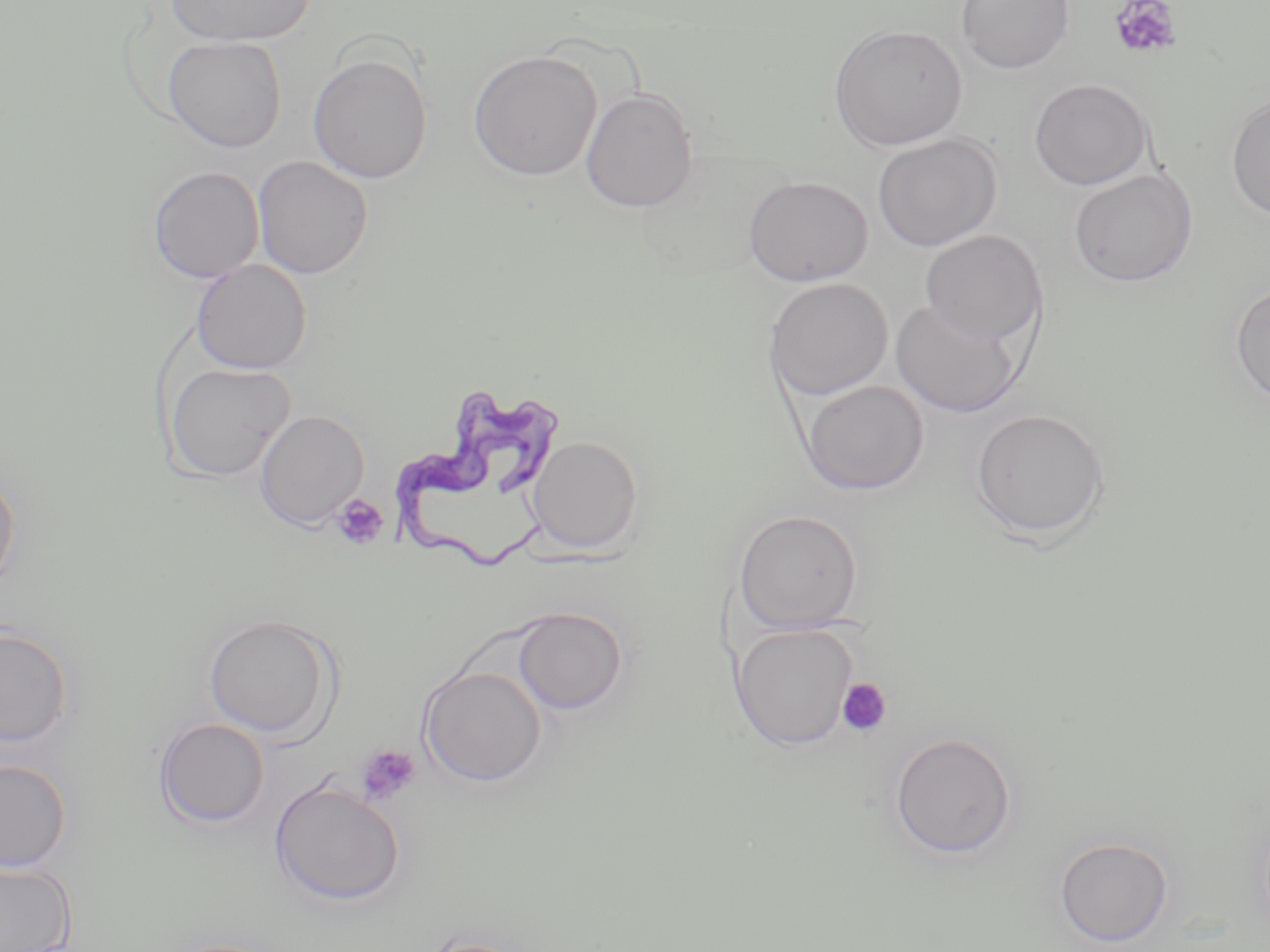
slide-level diagnosis = Trypanosoma brucei
platelet locations = approximate bounding boxes as named x1/y1/x2/y2 corners in pixels: (x1=1109, y1=0, x2=1183, y2=60), (x1=330, y1=494, x2=390, y2=551), (x1=835, y1=677, x2=893, y2=738), (x1=356, y1=745, x2=421, y2=806)
uninfected red blood cell locations = approximate bounding boxes as named x1/y1/x2/y2 corners in pixels: (x1=167, y1=0, x2=315, y2=47), (x1=956, y1=1, x2=1075, y2=74), (x1=828, y1=23, x2=968, y2=151), (x1=163, y1=35, x2=287, y2=152), (x1=468, y1=49, x2=601, y2=181), (x1=307, y1=53, x2=433, y2=184), (x1=1029, y1=77, x2=1154, y2=190), (x1=580, y1=88, x2=698, y2=212), (x1=1225, y1=93, x2=1270, y2=221), (x1=872, y1=133, x2=1003, y2=252), (x1=253, y1=156, x2=373, y2=279), (x1=147, y1=165, x2=265, y2=282), (x1=1068, y1=167, x2=1198, y2=288), (x1=743, y1=174, x2=874, y2=287), (x1=919, y1=229, x2=1047, y2=348), (x1=191, y1=259, x2=312, y2=375), (x1=763, y1=277, x2=894, y2=400), (x1=1230, y1=283, x2=1270, y2=409), (x1=890, y1=299, x2=1025, y2=418), (x1=164, y1=362, x2=295, y2=481), (x1=799, y1=380, x2=930, y2=496), (x1=968, y1=407, x2=1111, y2=542), (x1=255, y1=410, x2=369, y2=530), (x1=527, y1=435, x2=643, y2=554), (x1=0, y1=468, x2=20, y2=595), (x1=732, y1=509, x2=865, y2=633), (x1=512, y1=606, x2=629, y2=715), (x1=203, y1=614, x2=339, y2=739), (x1=731, y1=623, x2=859, y2=750), (x1=0, y1=624, x2=73, y2=747), (x1=418, y1=665, x2=547, y2=787), (x1=153, y1=717, x2=270, y2=829), (x1=889, y1=731, x2=1018, y2=860), (x1=0, y1=758, x2=72, y2=873), (x1=269, y1=779, x2=407, y2=908), (x1=1054, y1=836, x2=1174, y2=946), (x1=0, y1=860, x2=76, y2=952), (x1=413, y1=935, x2=546, y2=952)
preparation = thin blood film
stain = May-Grünwald-Giemsa
Trypanosoma brucei locations = approximate bounding boxes as named x1/y1/x2/y2 corners in pixels: (x1=389, y1=388, x2=567, y2=580)
field of view = one of a larger specimen
magnification = 1000x
image size = 1270×952 pixels
modality = optical microscopy